Outline each blood parasite and name the species.
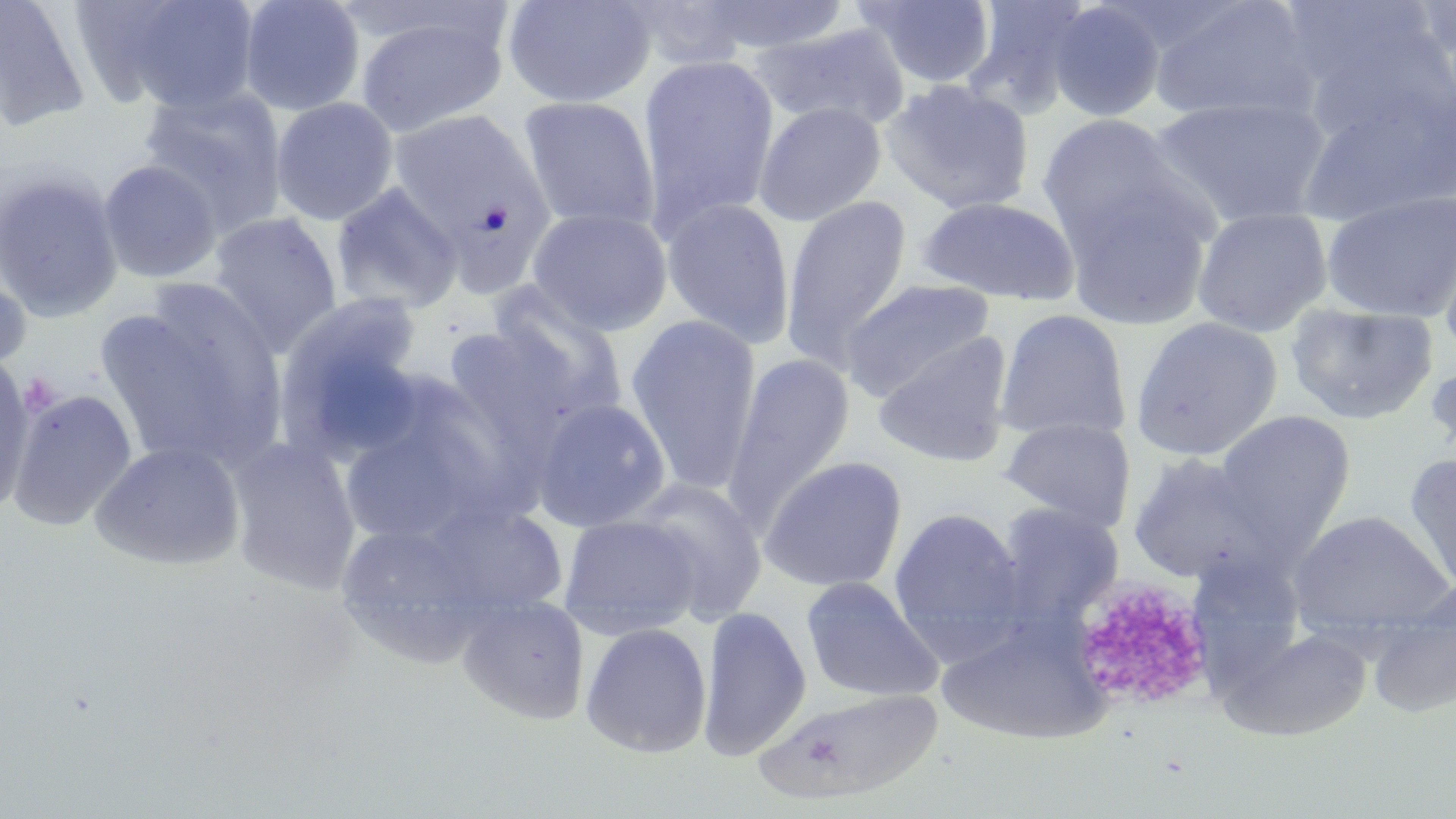

No blood parasites seen.

slide-level diagnosis = no evidence of blood parasites
uninfected red blood cell locations = approximate bounding boxes as (x1,y1)-(x2,y2) corner pairs in pixels: (0,0)-(91,133), (104,0)-(261,114), (238,0)-(366,116), (501,0)-(656,109), (692,0)-(852,55), (854,0)-(998,89), (960,0)-(1097,117), (1148,0)-(1319,125), (1048,1)-(1166,123), (616,2)-(766,68), (1284,4)-(1453,143), (354,9)-(511,138), (752,21)-(911,133), (636,53)-(780,239), (880,79)-(1035,215), (1293,82)-(1456,228), (138,86)-(288,235), (517,95)-(661,233), (1151,96)-(1332,227), (270,97)-(399,225), (753,102)-(886,226), (389,109)-(551,296), (1036,113)-(1191,252), (99,160)-(222,283), (0,170)-(123,322), (1059,181)-(1216,330), (331,183)-(463,314), (1320,191)-(1456,323), (779,195)-(913,370), (915,196)-(1080,306), (661,197)-(796,348), (526,207)-(673,336), (1191,207)-(1332,337), (208,212)-(343,356), (1436,220)-(1456,362), (0,268)-(31,377), (840,278)-(998,403), (484,286)-(628,427), (98,291)-(287,472), (274,293)-(428,460), (1285,302)-(1439,426), (994,308)-(1131,443), (624,314)-(763,494), (1130,316)-(1283,461), (871,331)-(1015,468), (722,352)-(856,531), (1424,358)-(1456,466), (0,363)-(37,512), (8,389)-(137,531), (530,398)-(671,533), (339,408)-(500,548), (1212,410)-(1357,551), (999,416)-(1136,530), (226,437)-(361,595), (90,440)-(247,571), (1126,452)-(1280,586), (1403,453)-(1455,598), (758,455)-(908,594), (627,478)-(767,624), (416,499)-(570,619), (993,503)-(1125,629), (888,506)-(1029,662), (1286,509)-(1455,643), (559,514)-(703,640), (331,518)-(501,668), (801,576)-(944,703), (1364,587)-(1456,719), (457,595)-(590,725), (696,606)-(812,761), (937,618)-(1109,745), (580,622)-(713,758), (1218,626)-(1372,742), (754,687)-(944,806)
platelet locations = approximate bounding boxes as (x1,y1)-(x2,y2) corner pairs in pixels: (1065,575)-(1216,712)
field of view = single
image size = 1456×819 pixels
modality = light microscopy
stain = May-Grünwald-Giemsa
magnification = 1000x
preparation = thin blood film